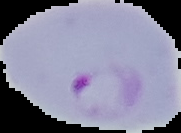

{
  "image_size": "181×133 pixels",
  "malaria_status": "parasitized",
  "image_type": "segmented cell region on a black background",
  "preparation": "thin blood film"
}